Classify this cell by malaria status.
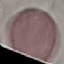

Uninfected.

Automatically extracted cell patch, resized to 64 × 64 pixels. Acquired by smartphone through the microscope eyepiece. Thin blood film. Giemsa-stained preparation.